Outline Plasmodium parasites and white blood cells.
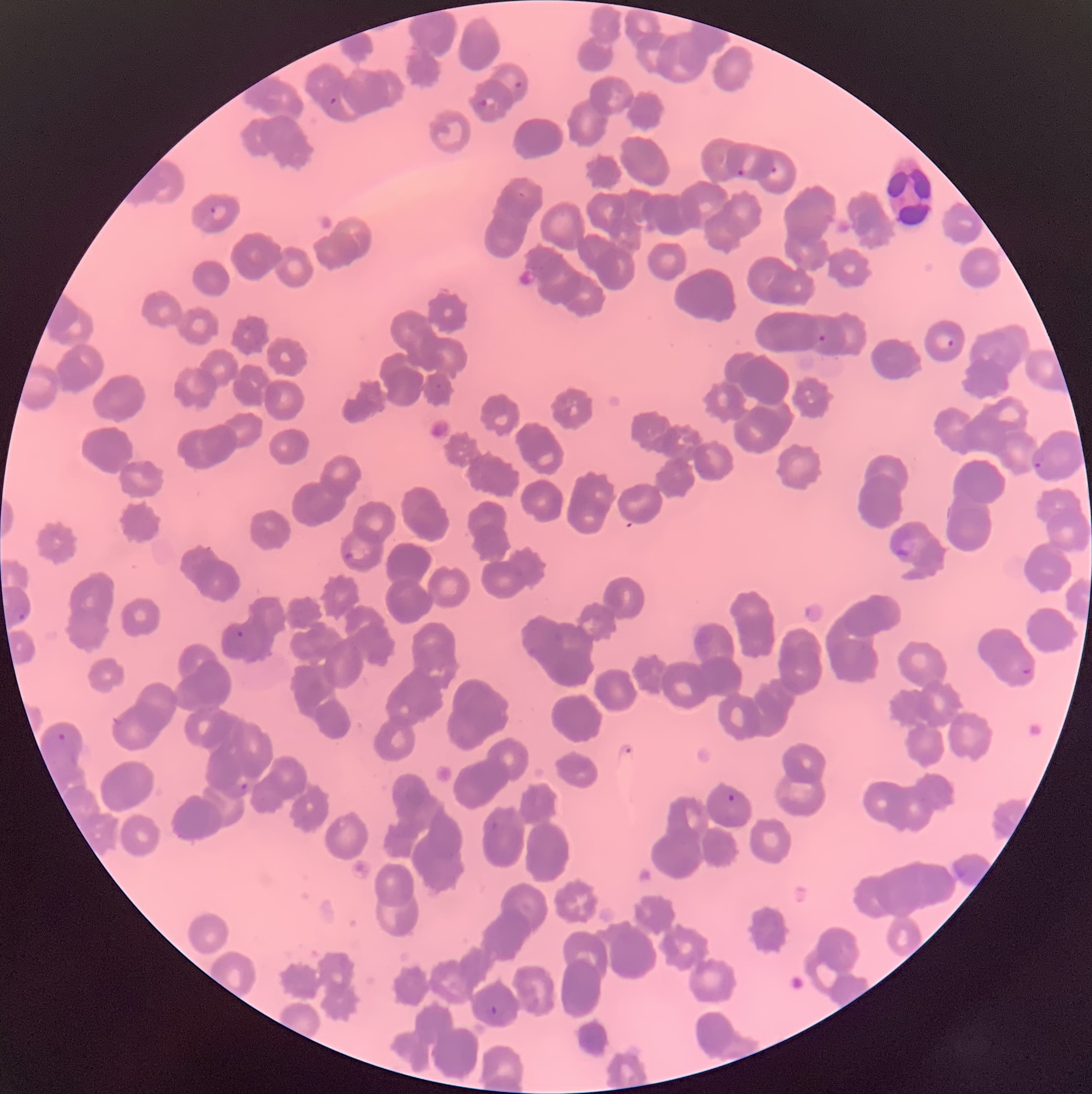

Approximate bounding boxes as (x1,y1)-(x2,y2) corner pairs in pixels.
Plasmodium parasites: (515,81)-(523,87), (476,99)-(487,106), (770,166)-(778,173), (573,213)-(585,220), (818,333)-(826,341), (933,333)-(954,348), (1032,452)-(1044,469), (894,539)-(915,556), (344,552)-(353,559), (513,568)-(523,576), (13,608)-(29,624), (231,624)-(248,639), (554,631)-(564,641), (526,645)-(538,656), (1022,668)-(1031,676), (58,733)-(66,740), (239,783)-(249,793), (727,794)-(735,803), (491,820)-(499,830), (487,1007)-(498,1017).
Plasmodium parasites too small for a box (approximate centers as (x,y) in pixels): (333,100), (740,172), (522,194), (213,210), (438,386).
White blood cells: (882,157)-(934,229).

{
  "modality": "light microscopy",
  "preparation": "thin blood smear",
  "image_size": "1092×1094 pixels",
  "red_blood_cell_morphology": "rouleaux formation"
}